Classify this cell by malaria status.
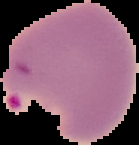
Parasitized.

image_type: cell region segmented out of the field of view; surrounding area masked to black
image_size: 139×145 pixels
preparation: thin blood smear